Assess this cell for malaria.
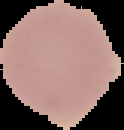

It is uninfected.

Summary:
  - Preparation: thin blood film
  - Image size: 124×130 pixels
  - Image type: segmented cell region on a black background